Describe the morphology of the red blood cells.
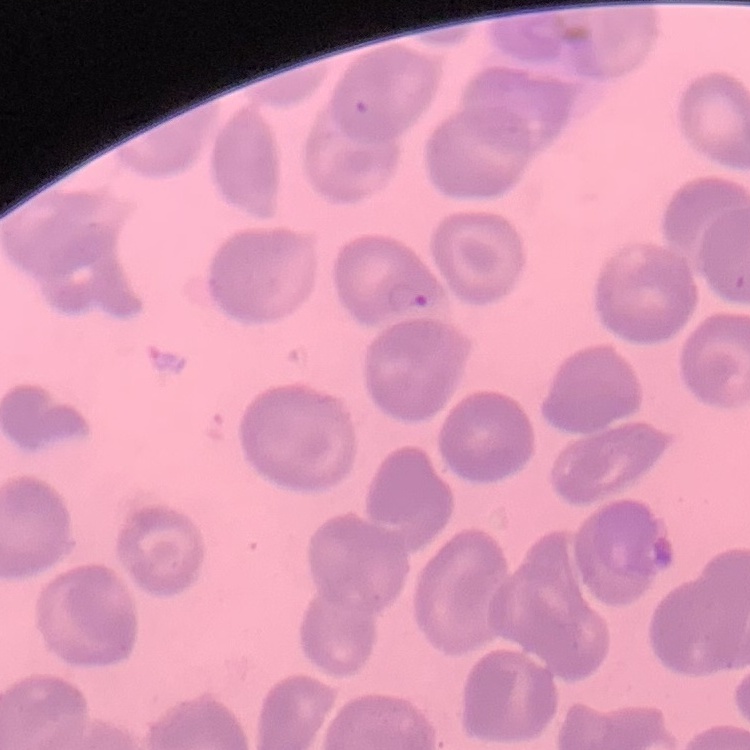

No rouleaux formation.

Summary:
  - Preparation: thin blood film
  - Stain: Field's or Giemsa
  - Image type: square crop of a larger photomicrograph